Give the extent of all uninfected red blood cells.
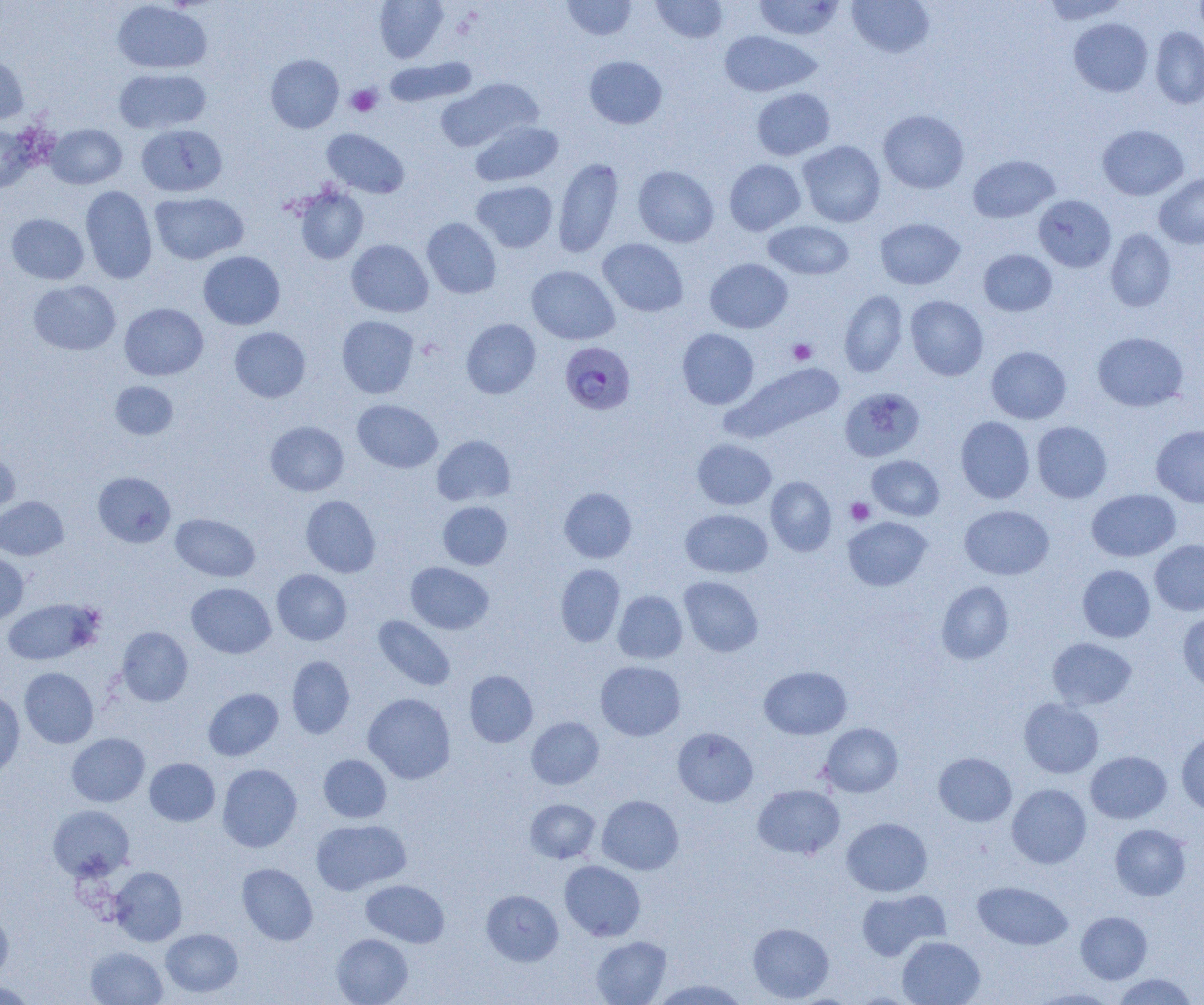
Approximate bounding boxes as named x1/y1/x2/y2 corners in pixels.
Uninfected red blood cells: (x1=374, y1=0, x2=448, y2=63), (x1=563, y1=0, x2=637, y2=40), (x1=651, y1=0, x2=728, y2=43), (x1=754, y1=0, x2=844, y2=40), (x1=847, y1=0, x2=935, y2=58), (x1=1042, y1=0, x2=1130, y2=23), (x1=112, y1=1, x2=212, y2=74), (x1=1069, y1=18, x2=1153, y2=97), (x1=1150, y1=27, x2=1204, y2=108), (x1=718, y1=30, x2=821, y2=97), (x1=0, y1=50, x2=29, y2=124), (x1=266, y1=54, x2=343, y2=133), (x1=584, y1=56, x2=667, y2=129), (x1=383, y1=57, x2=477, y2=107), (x1=113, y1=67, x2=211, y2=134), (x1=436, y1=78, x2=543, y2=151), (x1=752, y1=88, x2=835, y2=160), (x1=878, y1=109, x2=969, y2=193), (x1=470, y1=120, x2=563, y2=187), (x1=0, y1=124, x2=37, y2=192), (x1=46, y1=124, x2=127, y2=189), (x1=136, y1=124, x2=227, y2=197), (x1=1098, y1=125, x2=1189, y2=200), (x1=322, y1=129, x2=409, y2=198), (x1=798, y1=141, x2=886, y2=227), (x1=968, y1=155, x2=1060, y2=223), (x1=553, y1=157, x2=624, y2=258), (x1=724, y1=159, x2=806, y2=235), (x1=475, y1=165, x2=625, y2=255), (x1=633, y1=165, x2=719, y2=248), (x1=1154, y1=173, x2=1204, y2=249), (x1=472, y1=181, x2=558, y2=252), (x1=80, y1=185, x2=157, y2=283), (x1=292, y1=185, x2=368, y2=264), (x1=150, y1=192, x2=248, y2=264), (x1=1034, y1=195, x2=1115, y2=272), (x1=6, y1=214, x2=89, y2=284), (x1=422, y1=218, x2=501, y2=298), (x1=875, y1=218, x2=965, y2=290), (x1=763, y1=220, x2=854, y2=280), (x1=1105, y1=229, x2=1176, y2=312), (x1=597, y1=239, x2=688, y2=316), (x1=346, y1=240, x2=433, y2=317), (x1=979, y1=249, x2=1057, y2=316), (x1=198, y1=251, x2=285, y2=329), (x1=705, y1=258, x2=792, y2=333), (x1=526, y1=265, x2=619, y2=345), (x1=28, y1=280, x2=121, y2=355), (x1=839, y1=290, x2=908, y2=377), (x1=905, y1=295, x2=988, y2=380), (x1=119, y1=303, x2=208, y2=380), (x1=337, y1=315, x2=419, y2=398), (x1=461, y1=319, x2=540, y2=398), (x1=229, y1=327, x2=311, y2=402), (x1=677, y1=328, x2=759, y2=409), (x1=1092, y1=331, x2=1188, y2=411), (x1=986, y1=346, x2=1071, y2=424), (x1=726, y1=361, x2=846, y2=442), (x1=110, y1=381, x2=178, y2=439), (x1=840, y1=387, x2=925, y2=462), (x1=352, y1=399, x2=442, y2=473), (x1=956, y1=417, x2=1035, y2=503), (x1=265, y1=421, x2=349, y2=496), (x1=1032, y1=421, x2=1112, y2=502), (x1=1151, y1=424, x2=1204, y2=507), (x1=432, y1=435, x2=515, y2=506), (x1=692, y1=439, x2=776, y2=510), (x1=0, y1=444, x2=19, y2=518), (x1=867, y1=455, x2=944, y2=521), (x1=93, y1=471, x2=175, y2=547), (x1=766, y1=476, x2=836, y2=555), (x1=559, y1=487, x2=636, y2=563), (x1=1086, y1=488, x2=1181, y2=561), (x1=301, y1=495, x2=380, y2=577), (x1=0, y1=496, x2=68, y2=560), (x1=438, y1=501, x2=512, y2=569), (x1=959, y1=505, x2=1054, y2=579), (x1=680, y1=509, x2=772, y2=578), (x1=171, y1=513, x2=260, y2=582), (x1=843, y1=517, x2=932, y2=591), (x1=1149, y1=539, x2=1204, y2=615), (x1=0, y1=553, x2=29, y2=626), (x1=406, y1=562, x2=493, y2=634), (x1=555, y1=564, x2=625, y2=647), (x1=1077, y1=565, x2=1155, y2=642), (x1=272, y1=569, x2=351, y2=645), (x1=679, y1=576, x2=763, y2=656), (x1=936, y1=580, x2=1014, y2=665), (x1=186, y1=583, x2=275, y2=658), (x1=613, y1=590, x2=687, y2=664), (x1=2, y1=598, x2=101, y2=666), (x1=1178, y1=611, x2=1204, y2=692), (x1=373, y1=615, x2=455, y2=691), (x1=116, y1=626, x2=193, y2=706), (x1=1047, y1=637, x2=1137, y2=710), (x1=287, y1=655, x2=355, y2=739), (x1=595, y1=661, x2=685, y2=740), (x1=759, y1=665, x2=852, y2=739), (x1=19, y1=667, x2=99, y2=748), (x1=464, y1=670, x2=538, y2=747), (x1=203, y1=688, x2=283, y2=760), (x1=0, y1=689, x2=25, y2=780), (x1=363, y1=693, x2=455, y2=783), (x1=1019, y1=698, x2=1103, y2=778), (x1=526, y1=717, x2=604, y2=789), (x1=820, y1=723, x2=903, y2=797), (x1=672, y1=727, x2=758, y2=807), (x1=1176, y1=730, x2=1204, y2=814), (x1=67, y1=733, x2=150, y2=807), (x1=1085, y1=751, x2=1171, y2=823), (x1=933, y1=752, x2=1016, y2=826), (x1=318, y1=754, x2=391, y2=823), (x1=144, y1=758, x2=219, y2=826), (x1=217, y1=764, x2=302, y2=852), (x1=752, y1=784, x2=845, y2=859), (x1=1007, y1=784, x2=1091, y2=868), (x1=597, y1=795, x2=683, y2=875), (x1=525, y1=799, x2=600, y2=863), (x1=48, y1=804, x2=134, y2=881), (x1=841, y1=817, x2=932, y2=897), (x1=311, y1=819, x2=411, y2=895), (x1=1110, y1=824, x2=1191, y2=900), (x1=559, y1=860, x2=645, y2=941), (x1=237, y1=863, x2=318, y2=945), (x1=110, y1=866, x2=187, y2=946), (x1=361, y1=879, x2=449, y2=947), (x1=973, y1=881, x2=1072, y2=950), (x1=857, y1=889, x2=949, y2=960), (x1=481, y1=890, x2=563, y2=966), (x1=0, y1=909, x2=13, y2=984), (x1=1076, y1=911, x2=1152, y2=984), (x1=748, y1=922, x2=834, y2=1002), (x1=161, y1=928, x2=243, y2=997), (x1=331, y1=933, x2=412, y2=1005), (x1=590, y1=936, x2=671, y2=1005), (x1=897, y1=936, x2=985, y2=1005), (x1=85, y1=946, x2=168, y2=1004), (x1=1112, y1=973, x2=1199, y2=1004), (x1=649, y1=979, x2=750, y2=1004), (x1=0, y1=980, x2=38, y2=1004), (x1=1030, y1=988, x2=1120, y2=1004).

slide-level diagnosis = Plasmodium falciparum
preparation = thin blood smear
platelet locations = approximate bounding boxes as named x1/y1/x2/y2 corners in pixels: (x1=346, y1=84, x2=382, y2=117), (x1=788, y1=339, x2=816, y2=364), (x1=846, y1=498, x2=875, y2=525)
image size = 1204×1005 pixels
field of view = one of a larger specimen
magnification = 1000x
Plasmodium falciparum-infected red blood cell locations = approximate bounding boxes as named x1/y1/x2/y2 corners in pixels: (x1=560, y1=341, x2=636, y2=415)
modality = light microscopy